Name the cell type shown.
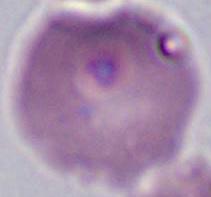

An erythrocyte.

Photomicrograph. Captured at 1000x magnification.